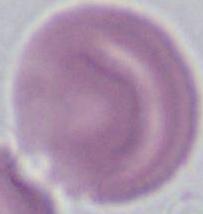
magnification = 1000x
identification = red blood cell
modality = micrograph